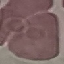

result = no malaria parasites seen
stain = Giemsa
image type = automatically extracted cell patch, resized to 64 × 64 pixels
preparation = thin blood film
capture = smartphone camera at the microscope eyepiece